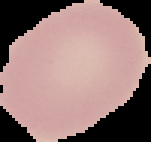

From a thin blood smear. Image is 151×142 pixels. Segmented cell region on a black background. Result: negative for Plasmodium parasites.